Give the position of every Plasmodium parasite visible.
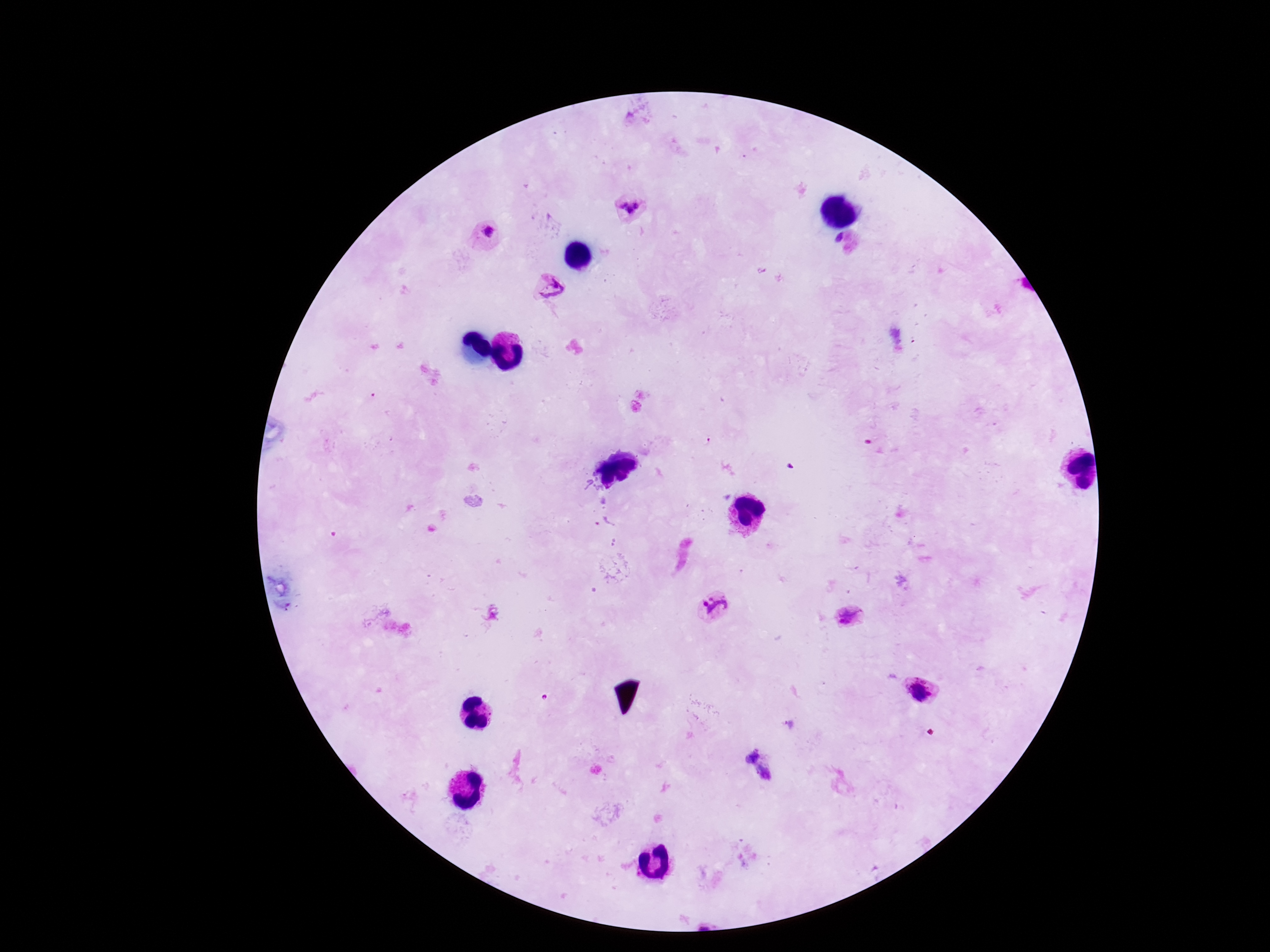

Approximate object centers, in pixels from the top-left corner.
Plasmodium parasites: (x=629, y=207), (x=485, y=233), (x=551, y=290), (x=713, y=607), (x=850, y=618), (x=918, y=688), (x=750, y=756), (x=766, y=775).

capture = smartphone camera through the microscope eyepiece
patient malaria status = positive
stain = Giemsa
field of view = one from this slide
magnification = 100x
image size = 1270×952 pixels
preparation = thick blood smear